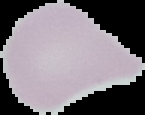

Summary:
  - Image size: 145×115 pixels
  - Preparation: thin blood film
  - Image type: segmented cell region with the area outside set to black
  - Result: no Plasmodium parasites seen